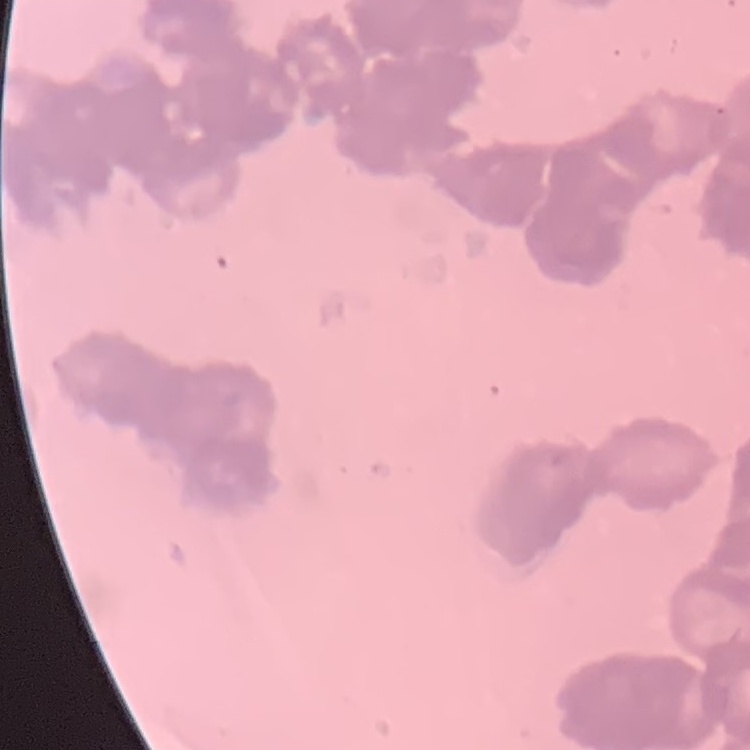

The red blood cells exhibit rouleaux formation. Thin blood smear. Square crop of a larger photomicrograph. Field's or Giemsa stain.